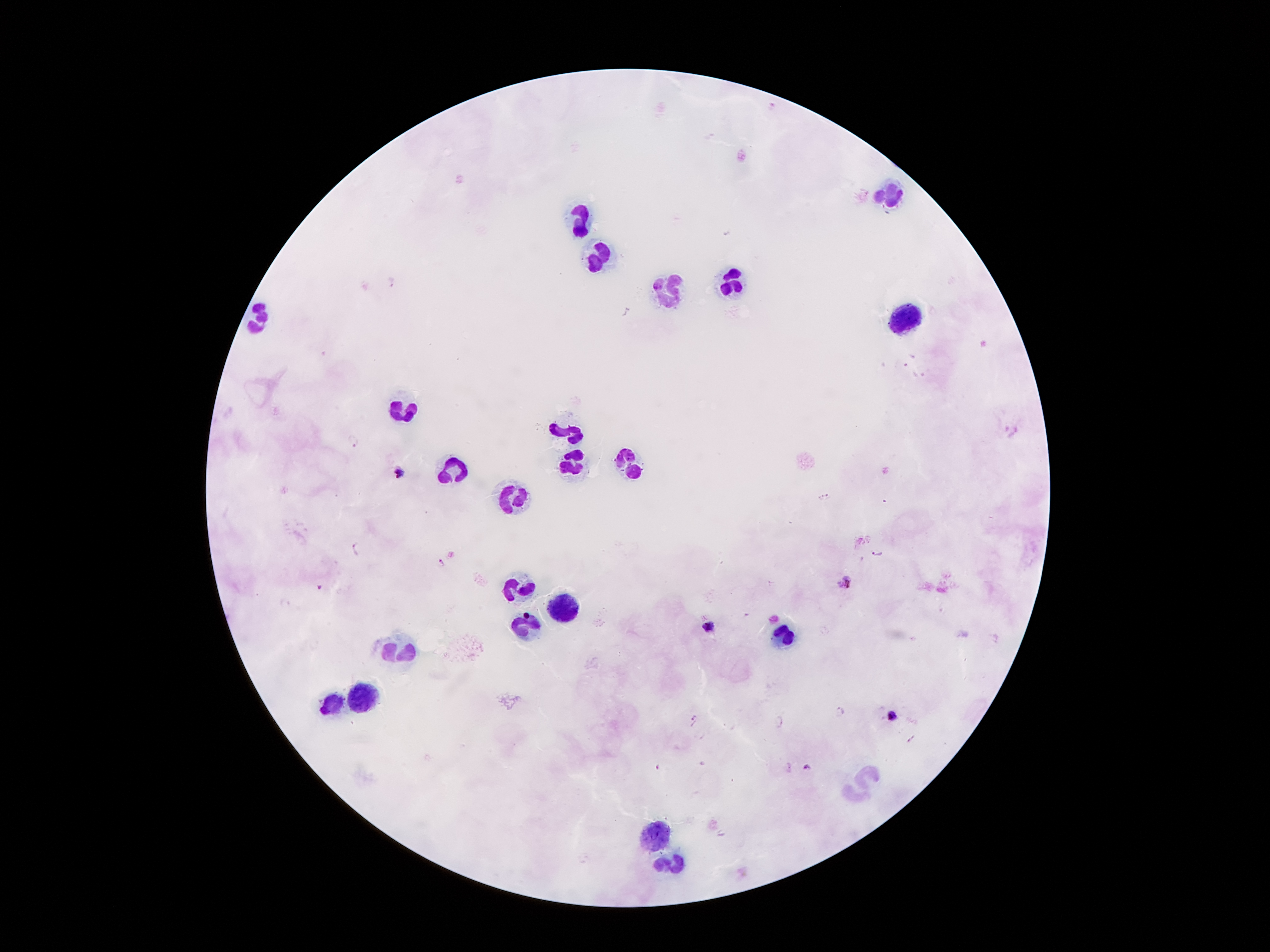

coordinate format = approximate object centers, in pixels from the top-left corner
leukocyte locations = (x=892, y=189), (x=578, y=215), (x=599, y=258), (x=737, y=282), (x=671, y=288), (x=257, y=316), (x=910, y=323), (x=399, y=411), (x=567, y=428), (x=574, y=463), (x=632, y=465), (x=455, y=471), (x=515, y=495), (x=518, y=588), (x=563, y=609), (x=526, y=626), (x=785, y=635), (x=395, y=650), (x=358, y=698), (x=328, y=704), (x=868, y=773), (x=851, y=796), (x=656, y=835), (x=677, y=865)
malaria parasite locations = (x=393, y=281), (x=913, y=354), (x=901, y=363), (x=920, y=376), (x=355, y=441), (x=399, y=474), (x=825, y=497), (x=886, y=500), (x=357, y=548), (x=878, y=553), (x=440, y=563), (x=845, y=583), (x=321, y=587), (x=709, y=628), (x=840, y=710), (x=892, y=715), (x=693, y=719), (x=780, y=722), (x=806, y=767), (x=657, y=768)
preparation = thick blood film
stain = Giemsa
patient malaria status = positive for Plasmodium falciparum
field of view = single
image size = 1270×952 pixels
capture = smartphone camera through the microscope eyepiece
magnification = 100x